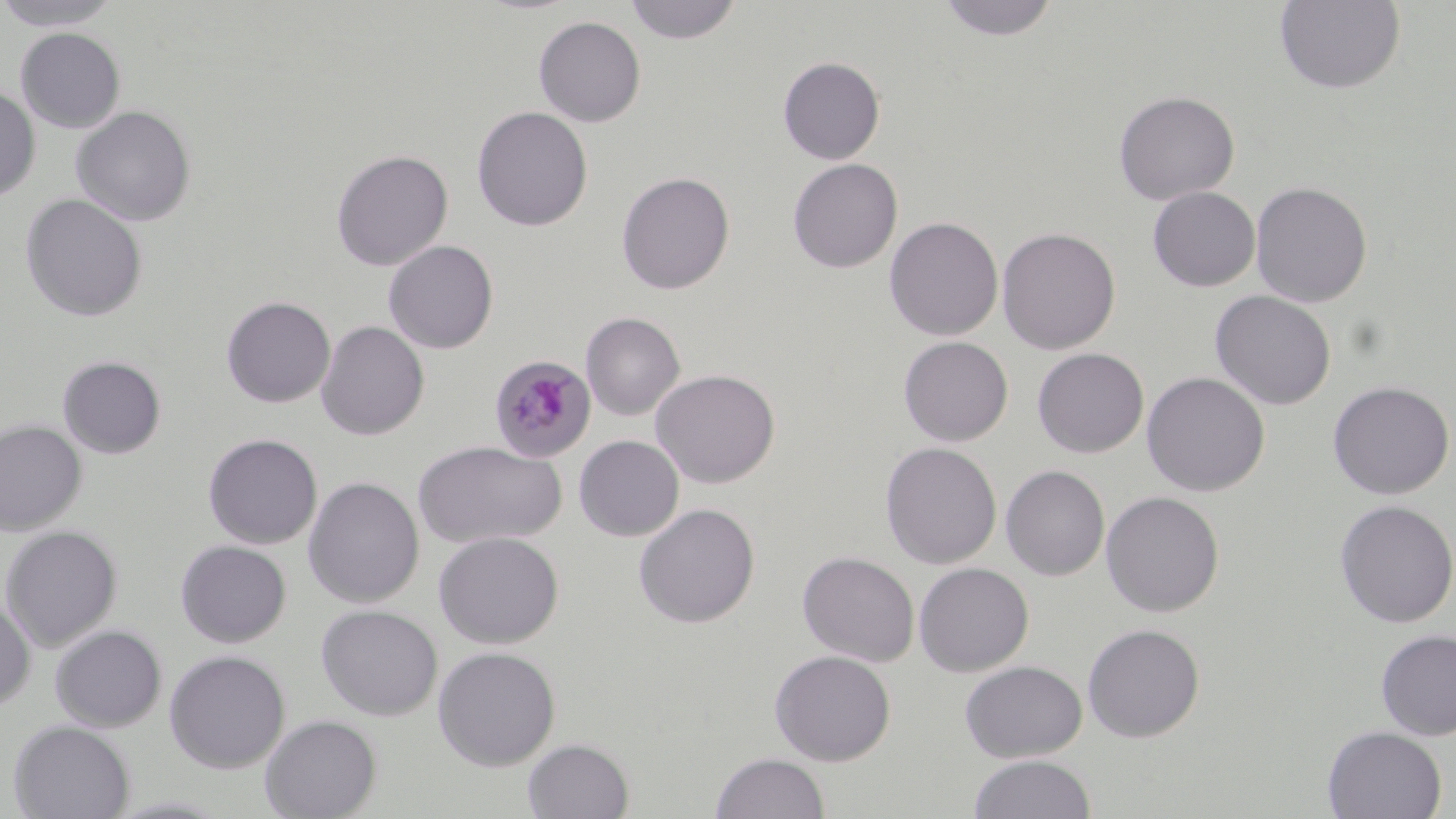

Approximate bounding boxes as [x1, y1, x2, y2] in pixels. Plasmodium malariae-infected red blood cell locations: [488, 354, 596, 462]. Uninfected red blood cell locations: [0, 0, 122, 31], [624, 0, 743, 44], [936, 0, 1060, 41], [1274, 0, 1406, 94], [533, 16, 646, 127], [15, 27, 126, 133], [777, 56, 885, 164], [0, 84, 40, 204], [1114, 91, 1240, 205], [71, 106, 196, 226], [472, 106, 593, 232], [332, 149, 453, 271], [787, 158, 903, 273], [616, 171, 735, 294], [1251, 181, 1372, 307], [1148, 187, 1261, 292], [20, 194, 148, 322], [884, 216, 1003, 340], [997, 226, 1121, 355], [384, 239, 498, 353], [1211, 290, 1336, 410], [221, 296, 336, 408], [581, 312, 685, 420], [316, 320, 429, 440], [898, 336, 1013, 446], [1032, 347, 1149, 458], [57, 355, 166, 459], [650, 369, 780, 488], [1141, 371, 1270, 497], [1327, 381, 1454, 500], [0, 419, 86, 536], [203, 433, 323, 549], [574, 435, 684, 541], [412, 440, 567, 548], [880, 442, 1002, 569], [1000, 465, 1109, 580], [303, 476, 424, 608], [1101, 491, 1224, 617], [1334, 499, 1456, 628], [634, 503, 760, 628], [0, 525, 122, 651], [433, 531, 563, 649], [175, 540, 291, 648], [797, 551, 919, 667], [913, 562, 1034, 677], [0, 595, 35, 713], [316, 604, 442, 721], [1082, 623, 1205, 742], [49, 624, 167, 732], [1375, 629, 1456, 741], [432, 646, 560, 772], [164, 650, 290, 774], [770, 650, 896, 766], [960, 660, 1087, 762], [260, 714, 381, 819], [8, 721, 135, 819], [1322, 725, 1447, 818], [523, 738, 635, 819], [711, 752, 829, 818], [967, 754, 1096, 818]. Slide-level diagnosis: Plasmodium malariae. May-Grünwald-Giemsa stain. Image is 1456×819 pixels. One field of a larger specimen. Optical microscopy. Thin blood film. 1000x magnification.